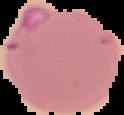
preparation = thin blood film
image type = cell region segmented out of the field of view; surrounding area masked to black
image size = 124×115 pixels
malaria status = parasitized